Locate every malaria parasite.
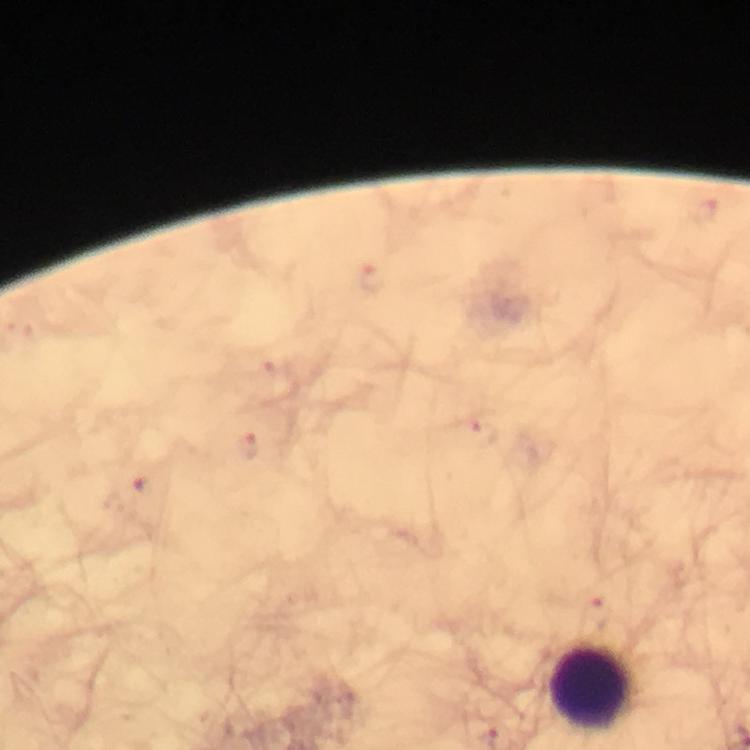
Approximate centers as [x, y] in pixels.
Malaria parasites: [706, 212], [372, 277], [271, 368], [482, 436], [248, 446], [143, 487], [600, 612].

Summary:
  - Leukocyte locations: [593, 688]
  - Stain: Giemsa
  - Cropped from: one field of view
  - Capture: smartphone photograph through a microscope
  - Magnification: 100x
  - Immersion oil: applied
  - Preparation: thick blood film
  - Context: from a diagnostic examination for malaria
  - Image size: 750×750 pixels